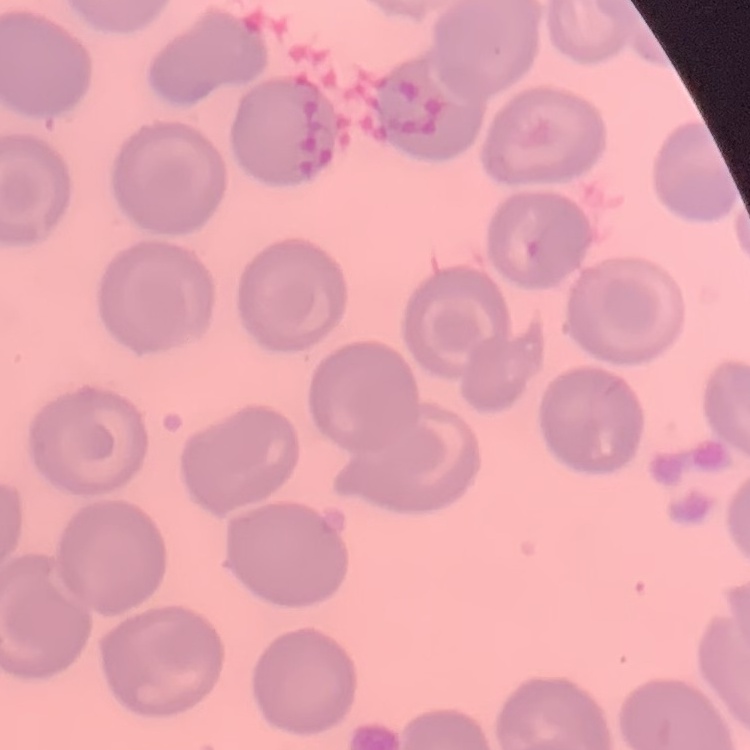
red_blood_cell_morphology: no rouleaux formation
stain: Field's or Giemsa
image_type: square crop of a larger photomicrograph
preparation: thin peripheral smear